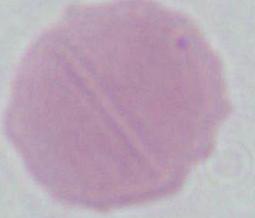
identification = red blood cell
modality = photomicrograph
magnification = 1000x